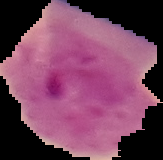
{
  "image_size": "163×160 pixels",
  "result": "Plasmodium parasites identified",
  "image_type": "cell region segmented out of the field of view; surrounding area masked to black",
  "preparation": "thin blood smear"
}